Assess this cell for malaria.
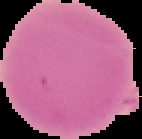

Uninfected.

The area outside the segmented cell region is set to black. Image is 142×139 pixels. From a thin blood smear.